Identify the preparation type.
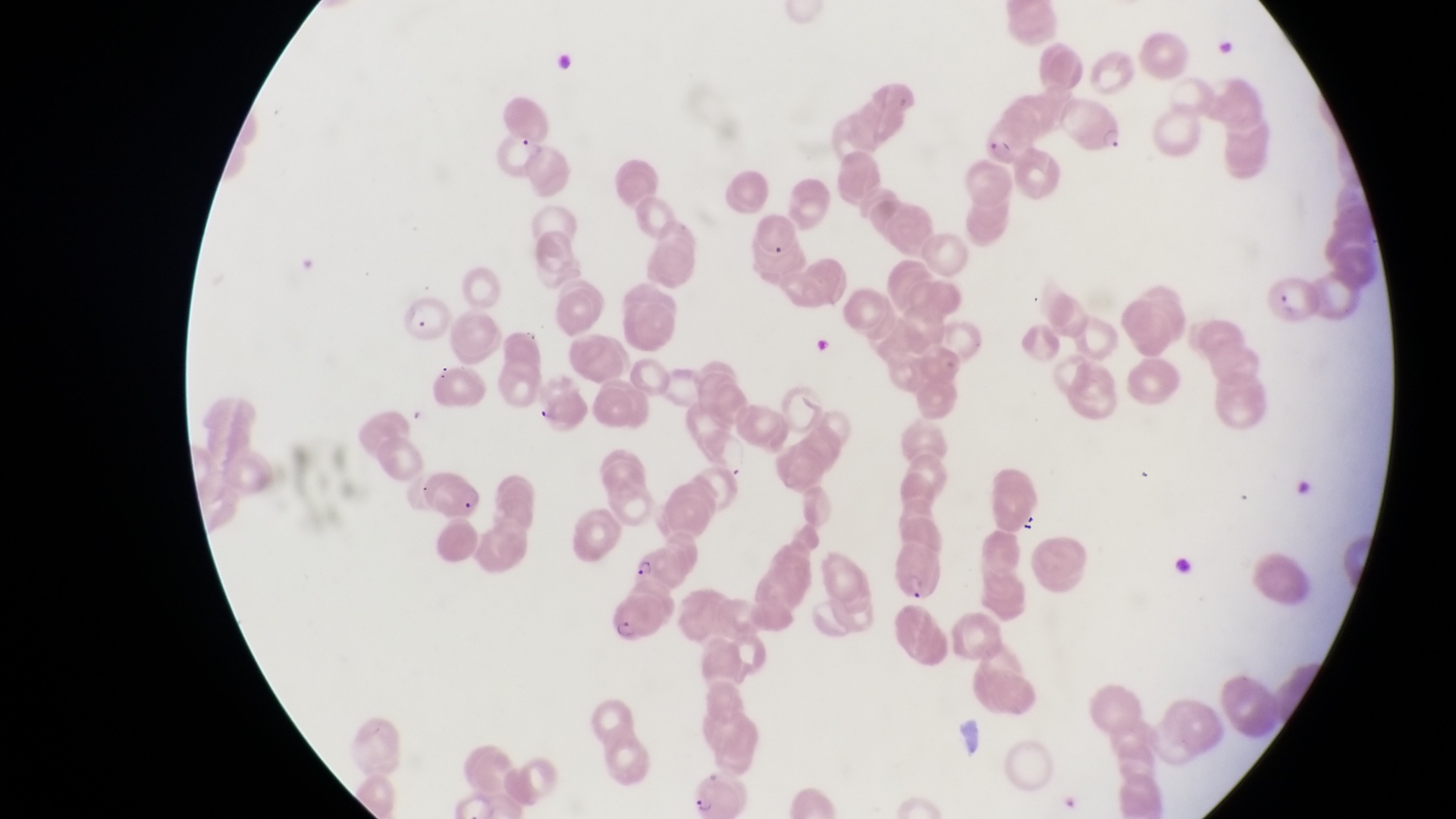

Thin blood film.

Approximate bounding boxes as left top right bottom in pixels.
Summary:
  - Parasitised red blood cell locations: 1062 98 1130 159; 495 130 551 177; 421 466 487 512; 899 541 944 601; 632 544 692 597; 608 587 668 645; 695 770 758 817
  - Object labeled both artifact (platelet-like body, stain precipitate, or debris) and parasitised red blood cell by the source: 986 122 1041 177
  - Artifact (platelet-like body, stain precipitate, or debris) locations: 1294 472 1321 501; 1021 515 1042 538; 1172 544 1198 581
  - Magnification: 1000x
  - Capture: smartphone photograph through the eyepiece of an Olympus CX-23 microscope
  - Field of view: single
  - Image size: 1456×819 pixels
  - Country: Uganda